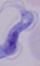

Photomicrograph. A trypanosome is seen. Captured at 1000x magnification.